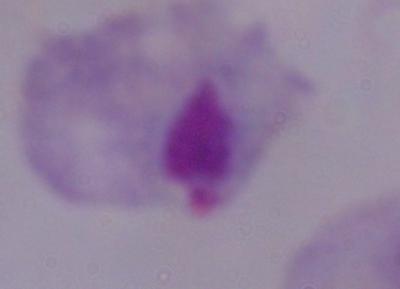

magnification = 1000x
modality = micrograph
identification = trichomonad